Name the blood parasite species.
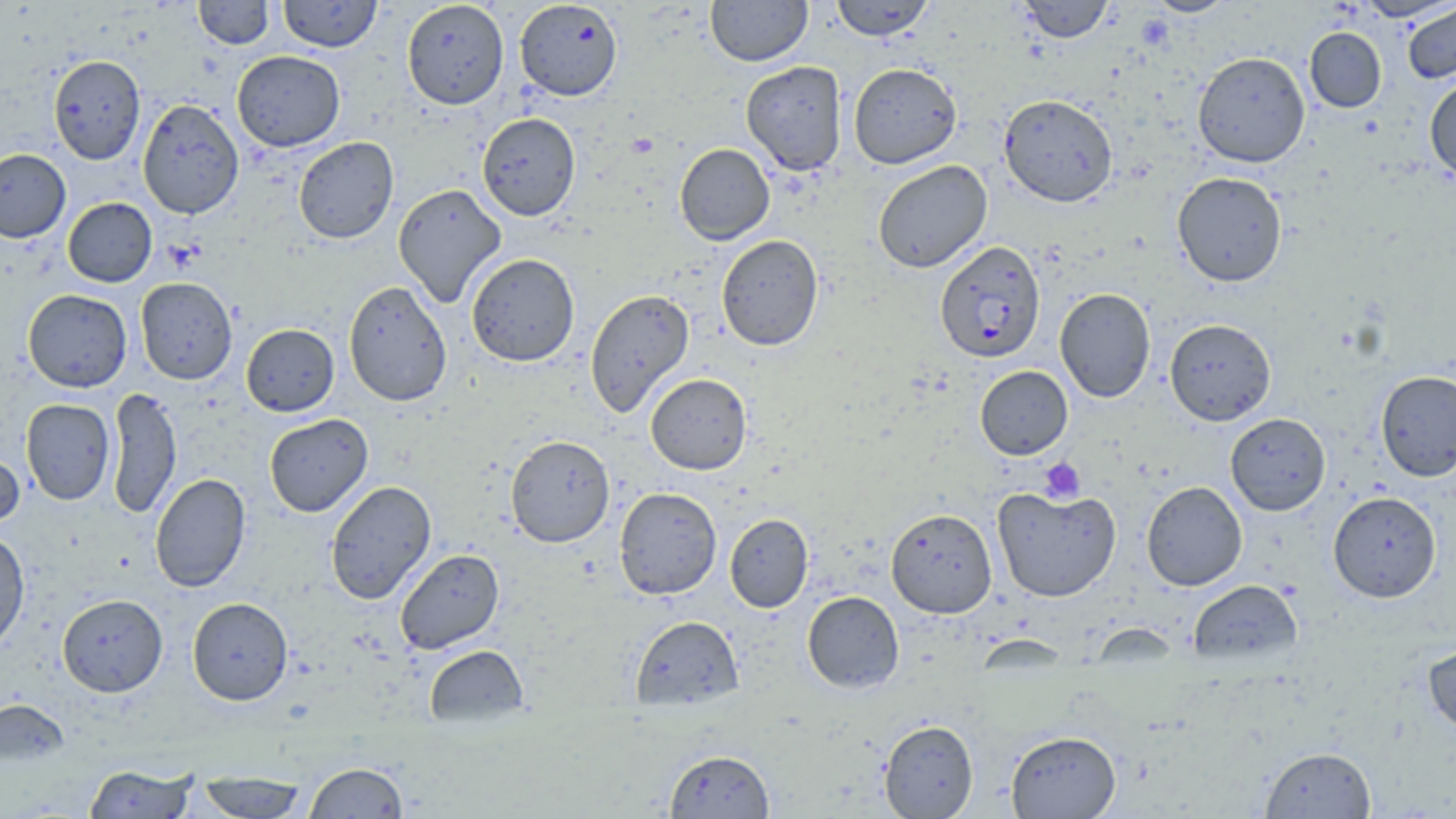

Plasmodium falciparum.

Summary:
  - Coordinate format: approximate bounding boxes as (x1, y1, x2, y2) in pixels
  - Platelet locations: (1040, 457, 1086, 503)
  - Plasmodium falciparum-infected red blood cell locations: (934, 240, 1045, 363)
  - Uninfected red blood cell locations: (194, 0, 274, 49), (278, 0, 382, 52), (706, 0, 812, 66), (830, 0, 935, 41), (1017, 0, 1113, 43), (1144, 0, 1237, 17), (401, 1, 509, 109), (514, 1, 623, 101), (1403, 3, 1456, 84), (1304, 27, 1386, 113), (232, 50, 345, 152), (1192, 51, 1310, 168), (48, 55, 145, 165), (741, 60, 848, 176), (848, 63, 962, 169), (1424, 77, 1456, 182), (999, 93, 1117, 207), (137, 99, 244, 219), (477, 112, 581, 220), (293, 137, 399, 243), (675, 143, 775, 245), (0, 148, 71, 243), (872, 160, 992, 273), (1172, 172, 1287, 287), (392, 183, 507, 307), (63, 197, 157, 287), (716, 235, 823, 350), (466, 253, 580, 367), (135, 277, 237, 385), (343, 281, 452, 406), (1055, 287, 1155, 402), (585, 288, 694, 417), (22, 289, 132, 392), (1164, 319, 1276, 425), (241, 324, 339, 416), (975, 366, 1072, 460), (1375, 370, 1456, 481), (645, 373, 751, 475), (106, 387, 182, 519), (20, 399, 115, 505), (1225, 412, 1331, 515), (264, 413, 373, 516), (505, 434, 615, 548), (0, 447, 25, 532), (150, 473, 251, 592), (324, 480, 436, 605), (1141, 481, 1247, 591), (992, 486, 1121, 602), (614, 487, 722, 600), (1328, 491, 1442, 602), (885, 507, 997, 618), (724, 513, 814, 613), (0, 529, 30, 654), (395, 548, 505, 654), (1188, 579, 1304, 667), (802, 591, 904, 693), (58, 594, 168, 696), (187, 597, 293, 705), (629, 615, 744, 711), (1422, 641, 1456, 735), (424, 644, 528, 728), (0, 698, 69, 767), (878, 719, 979, 818), (1005, 730, 1121, 818), (1259, 745, 1377, 818), (664, 748, 775, 818), (303, 762, 409, 818), (83, 763, 197, 818), (195, 773, 309, 818)
  - Stain: May-Grünwald-Giemsa
  - Modality: light microscopy
  - Field of view: single
  - Preparation: thin blood film
  - Magnification: 1000x
  - Image size: 1456×819 pixels